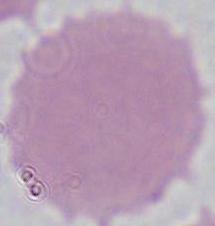

Summary:
  - Identification: erythrocyte
  - Magnification: 1000x
  - Modality: photomicrograph